Report the malaria status of this cell.
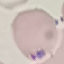

Parasitized.

Summary:
  - Image type: automatically extracted cell patch, resized to 64 × 64 pixels
  - Capture: smartphone camera at the microscope eyepiece
  - Stain: Giemsa
  - Preparation: thin blood smear